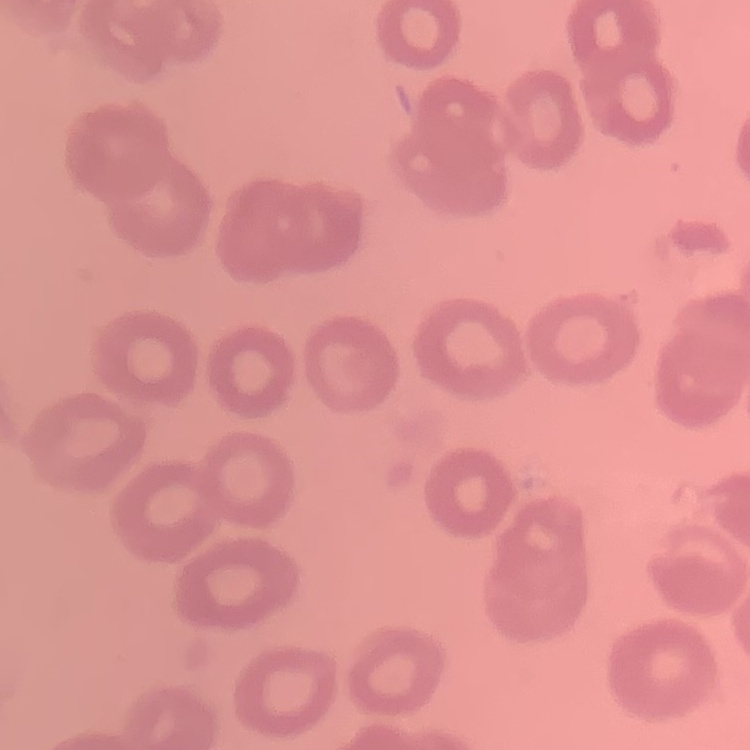
Summary:
  - Red blood cell morphology: no rouleaux formation
  - Image type: square crop of a larger photomicrograph
  - Preparation: thin blood smear
  - Stain: Field's or Giemsa